Classify this cell by malaria status.
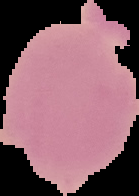

It is uninfected.

Summary:
  - Image size: 139×196 pixels
  - Image type: cell region segmented out of the field of view; surrounding area masked to black
  - Preparation: thin blood film